Report the malaria status of this cell.
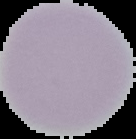

It is uninfected.

Summary:
  - Preparation: thin blood smear
  - Image type: segmented cell region on a black background
  - Image size: 136×139 pixels